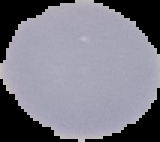
Segmented cell region on a black background. From a thin blood smear. Malaria status: uninfected. Image is 160×142 pixels.